Describe the morphology of the red blood cells.
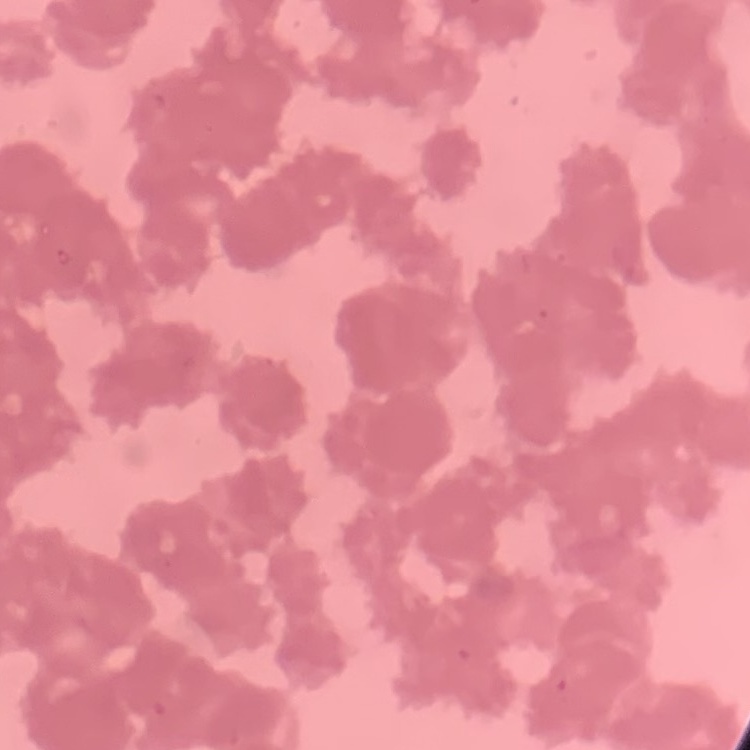

They show rouleaux formation.

Summary:
  - Preparation: thin blood film
  - Stain: Field's or Giemsa
  - Image type: square crop of a larger photomicrograph